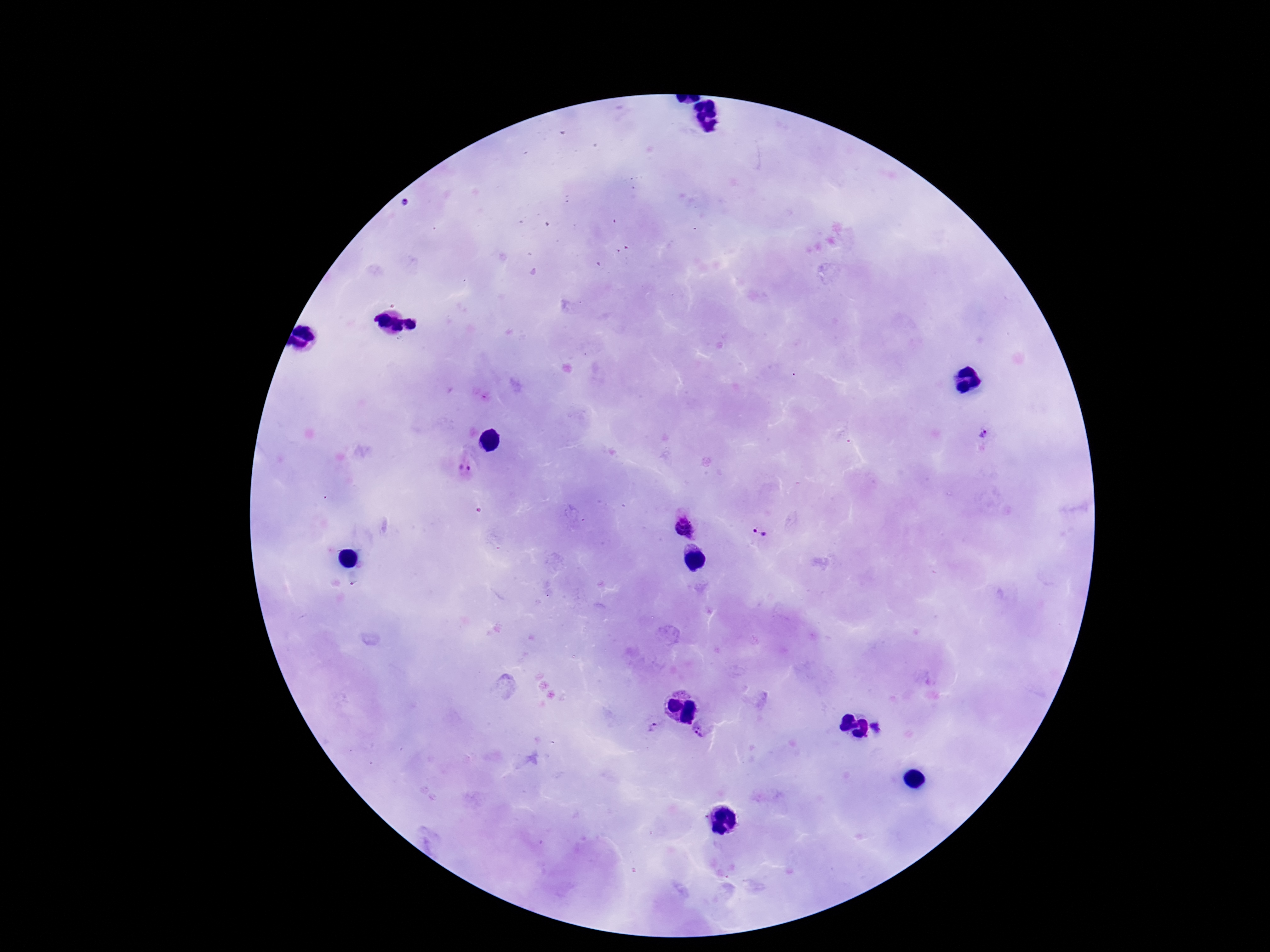
image size = 1270×952 pixels
patient malaria status = positive
Plasmodium parasite locations = approximate centers as [x, y] in pixels: [984, 434], [467, 462], [685, 525], [758, 533], [654, 726], [878, 727], [704, 728]
preparation = thick blood film
magnification = 100x
capture = smartphone camera through the microscope eyepiece
field of view = single
stain = Giemsa